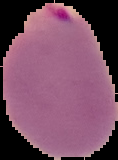

Summary:
  - Image size: 118×160 pixels
  - Result: malaria parasites identified
  - Preparation: thin blood smear
  - Image type: cell region segmented out of the field of view; surrounding area masked to black